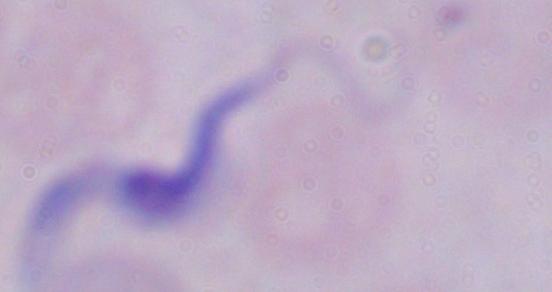
A trypanosome is seen. Micrograph. Captured at 1000x magnification.